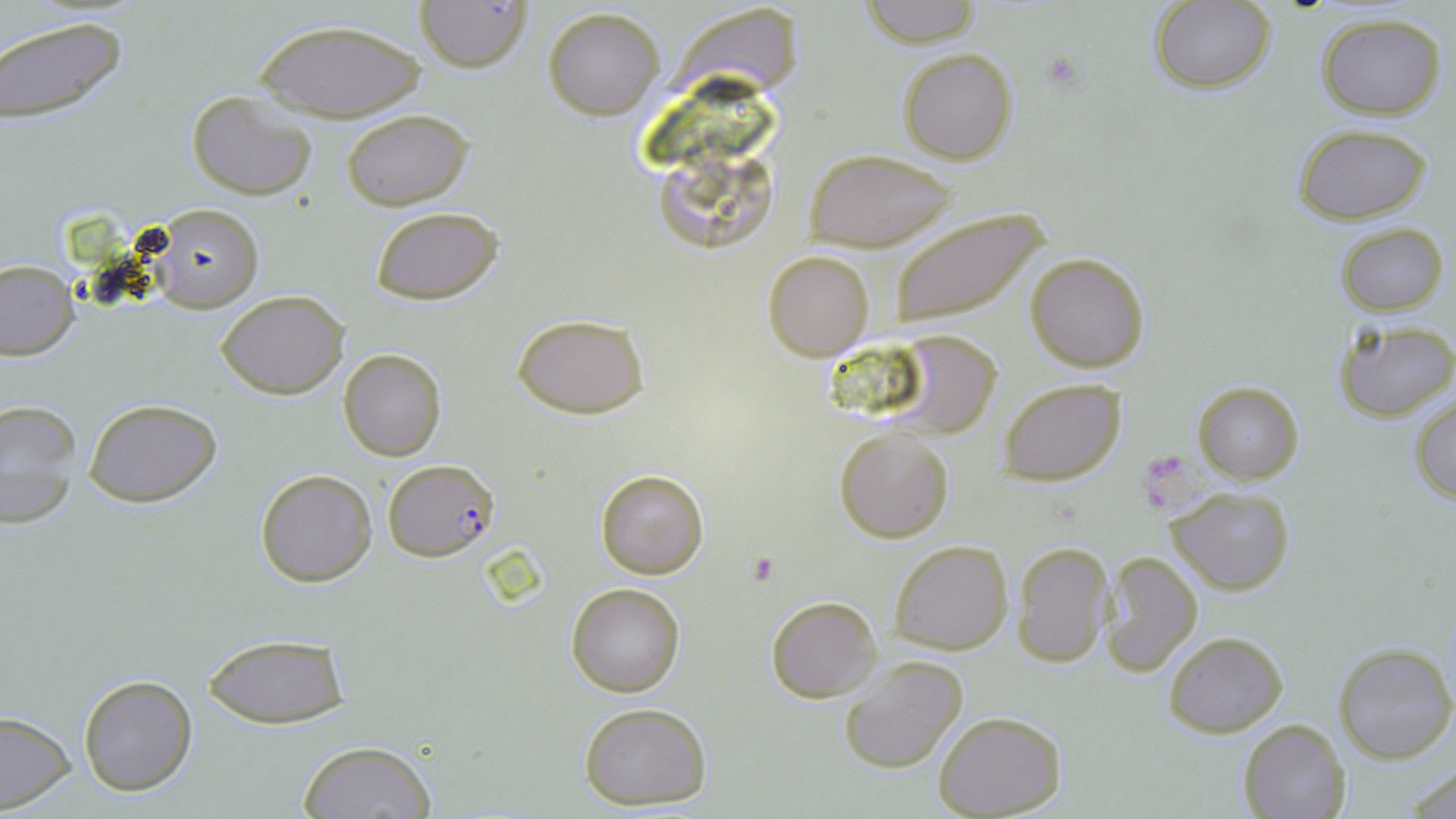
Summary:
  - Coordinate format: approximate bounding boxes as [x1, y1, x2, y2] in pixels
  - Plasmodium falciparum-infected red blood cell locations: [383, 458, 498, 563]
  - Platelet locations: [1041, 51, 1083, 92]
  - Uninfected red blood cell locations: [855, 0, 985, 47], [415, 1, 532, 72], [1147, 2, 1276, 94], [542, 6, 665, 120], [1315, 13, 1447, 119], [0, 15, 128, 128], [251, 18, 429, 124], [897, 47, 1017, 163], [187, 89, 318, 201], [341, 108, 474, 210], [1292, 124, 1433, 226], [806, 147, 957, 250], [149, 204, 263, 311], [369, 206, 505, 306], [887, 207, 1048, 330], [1335, 222, 1449, 316], [762, 249, 876, 361], [1023, 251, 1151, 373], [0, 259, 78, 361], [217, 288, 349, 399], [512, 314, 650, 419], [1332, 319, 1455, 420], [887, 330, 1004, 439], [339, 349, 447, 462], [998, 380, 1127, 485], [1192, 381, 1304, 485], [1409, 394, 1456, 506], [83, 397, 223, 506], [2, 398, 81, 530], [834, 428, 954, 543], [255, 468, 378, 588], [595, 468, 709, 580], [1166, 487, 1297, 596], [889, 539, 1014, 655], [1011, 541, 1115, 669], [1099, 550, 1203, 676], [566, 582, 686, 698], [766, 596, 881, 701], [1164, 631, 1288, 736], [204, 634, 350, 730], [1331, 641, 1456, 764], [837, 655, 968, 775], [78, 674, 197, 795], [577, 701, 714, 808], [0, 711, 75, 813], [935, 712, 1066, 818], [1239, 717, 1352, 819], [296, 739, 437, 818], [1403, 763, 1456, 817]
  - Slide-level diagnosis: Plasmodium falciparum
  - Preparation: thin blood film
  - Image size: 1456×819 pixels
  - Modality: optical microscopy
  - Stain: May-Grünwald-Giemsa
  - Field of view: single
  - Magnification: 1000x